Evaluate for malaria.
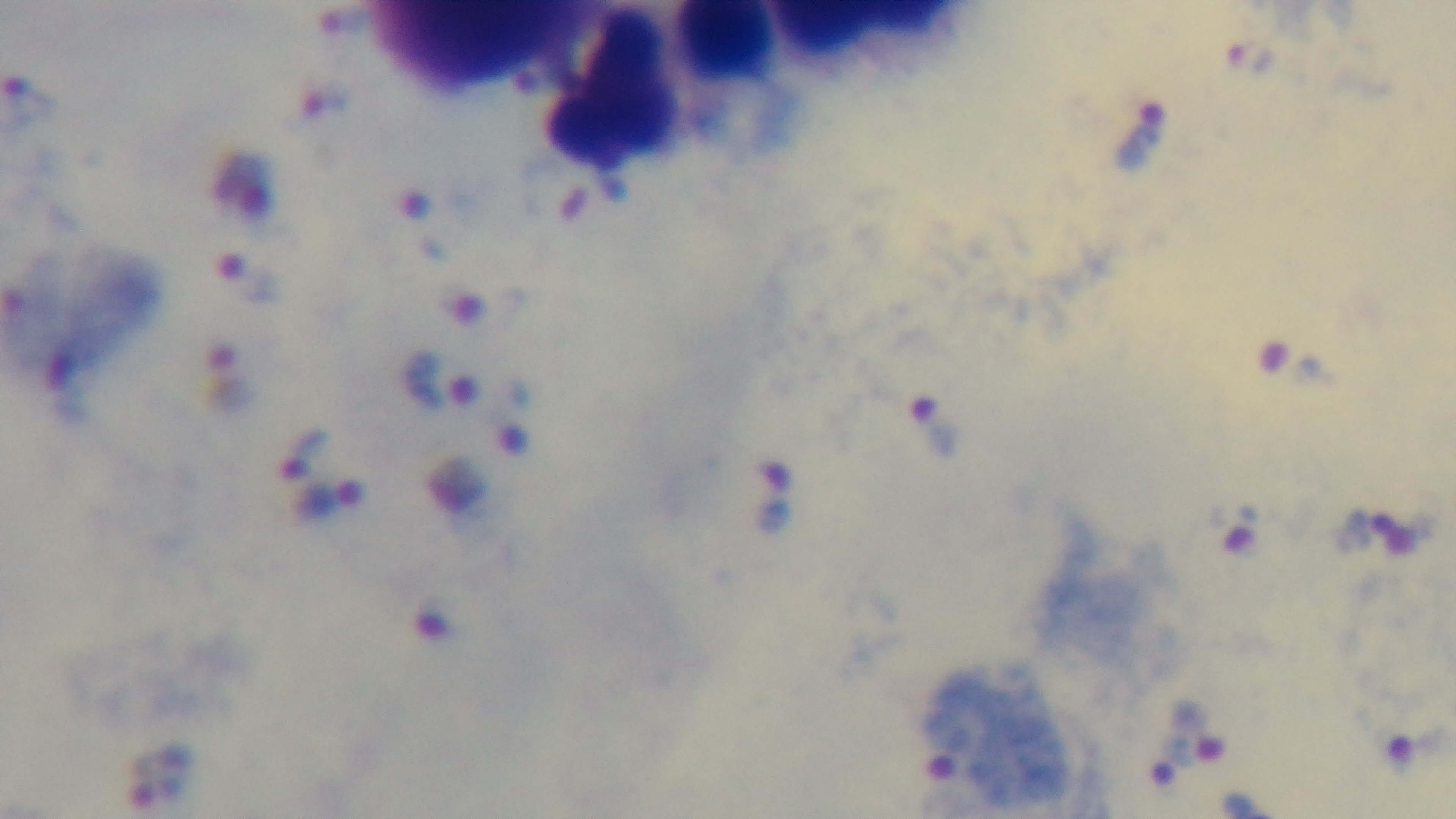
Infected.

Preparation: thick smear. Oil-immersion objective, 100x. Captured with a mounted 4K digital camera. Giemsa stain. Photomicrograph. One field from the slide.